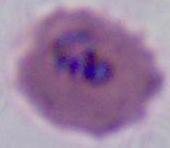

Summary:
  - Modality: photomicrograph
  - Magnification: 400x or 1000x
  - Identification: Plasmodium